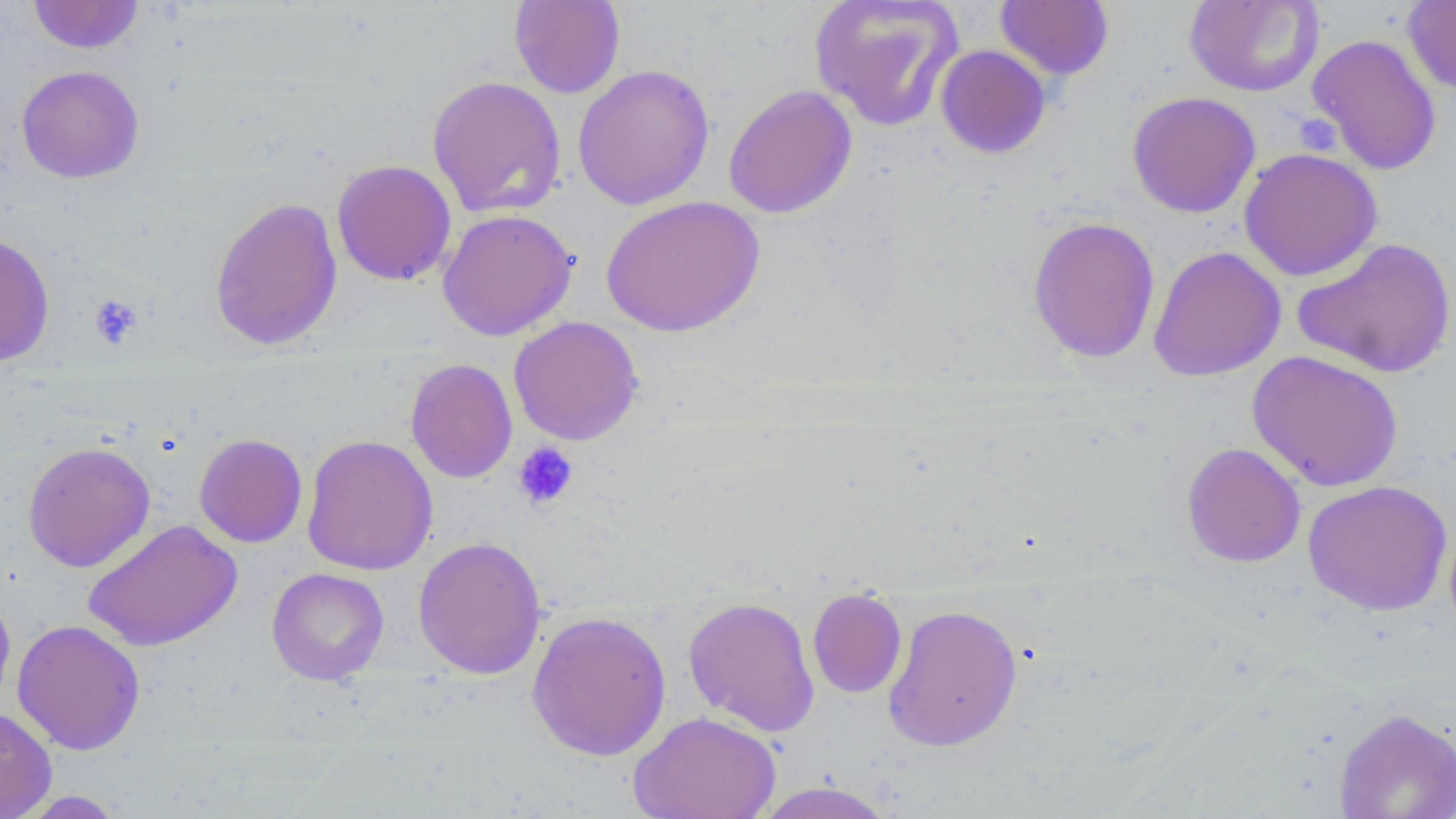
slide-level diagnosis = negative for blood parasites
image size = 1456×819 pixels
platelet locations = approximate bounding boxes as [x1, y1, x2, y2] in pixels: [1298, 116, 1343, 157], [88, 294, 144, 348], [512, 441, 579, 510]
modality = optical microscopy
field of view = one of a larger specimen
uninfected red blood cell locations = approximate bounding boxes as [x1, y1, x2, y2] in pixels: [27, 0, 144, 54], [509, 0, 626, 99], [808, 0, 965, 132], [1184, 0, 1324, 97], [1402, 0, 1456, 96], [994, 1, 1115, 80], [1306, 32, 1442, 176], [935, 45, 1051, 159], [572, 64, 715, 210], [16, 65, 144, 183], [426, 74, 567, 219], [723, 84, 858, 219], [1126, 91, 1261, 218], [1238, 148, 1382, 281], [331, 159, 457, 286], [600, 195, 765, 337], [209, 196, 344, 351], [437, 209, 578, 341], [1027, 216, 1161, 363], [0, 232, 55, 367], [1292, 236, 1456, 379], [1148, 246, 1286, 382], [508, 316, 644, 446], [1247, 350, 1404, 492], [405, 358, 518, 483], [194, 432, 308, 548], [301, 433, 438, 576], [22, 441, 155, 572], [1181, 442, 1306, 568], [1303, 480, 1452, 616], [82, 519, 242, 652], [413, 535, 546, 680], [267, 567, 390, 685], [807, 587, 908, 699], [0, 588, 16, 712], [682, 595, 820, 737], [882, 603, 1023, 752], [526, 610, 672, 761], [12, 618, 146, 755], [0, 706, 57, 819], [1334, 707, 1456, 819], [627, 710, 781, 819], [752, 781, 898, 819], [13, 790, 129, 818]
preparation = thin blood smear
stain = May-Grünwald-Giemsa
magnification = 1000x